State which parasite is depicted.
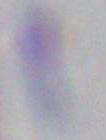

This is Toxoplasma gondii.

modality = photomicrograph
magnification = 1000x